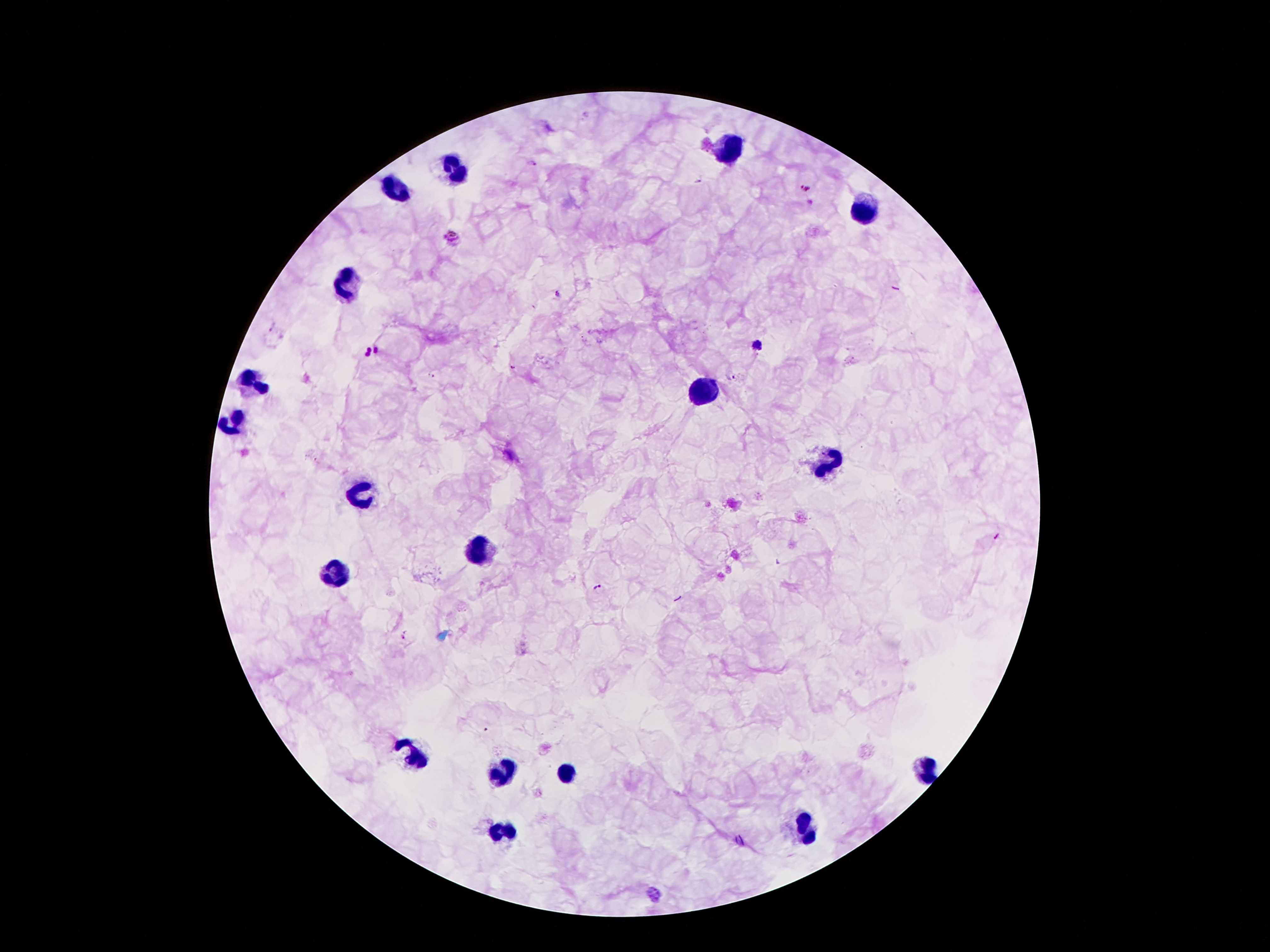

Approximate centers as (x, y) in pixels.
Summary:
  - Plasmodium parasite locations: (531, 163), (698, 182), (805, 187), (453, 236), (560, 294), (757, 345), (377, 349), (365, 352), (515, 366), (429, 375), (732, 375), (599, 587), (404, 633), (655, 893)
  - Leukocyte locations: (730, 148), (453, 167), (396, 186), (864, 211), (344, 286), (253, 381), (703, 389), (232, 423), (828, 461), (358, 494), (478, 545), (341, 572), (413, 753), (925, 772), (564, 774), (499, 776), (503, 830), (807, 830)
  - Stain: Giemsa
  - Preparation: thick peripheral-blood smear
  - Capture: smartphone through the microscope eyepiece
  - Patient malaria status: positive for Plasmodium falciparum
  - Field of view: single
  - Magnification: 100x
  - Image size: 1270×952 pixels